Assess the morphology of the erythrocytes.
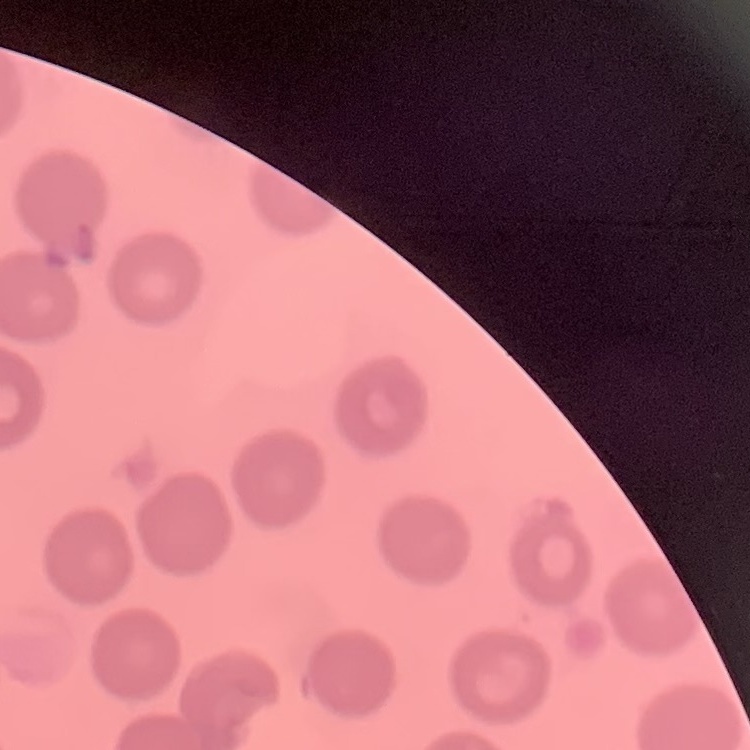
They show no rouleaux formation.

Stained with either Field's or Giemsa. Square crop of a larger photomicrograph. Thin blood film.